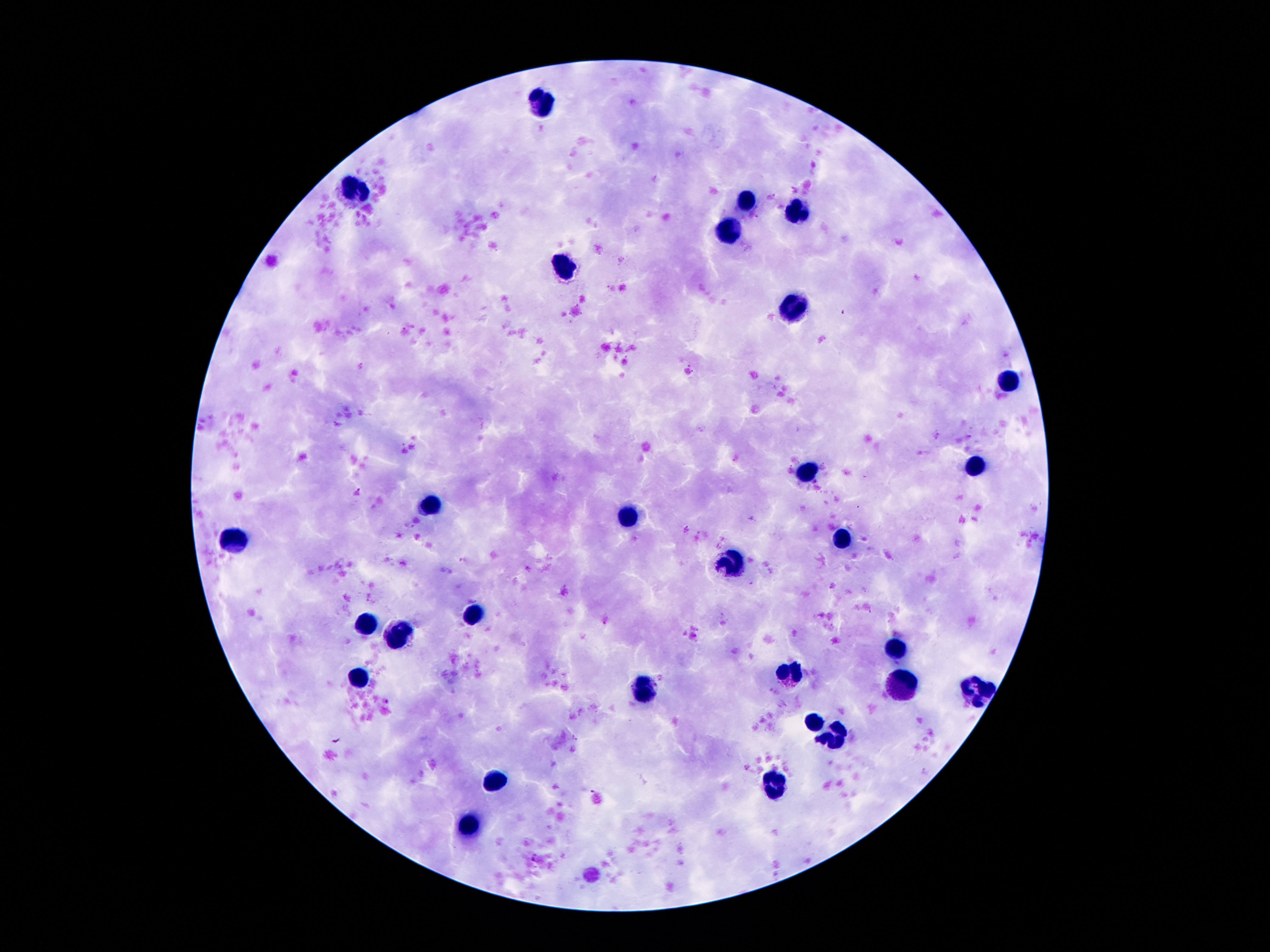 Approximate centers as {x, y} in pixels. Leukocyte locations: {545, 102}, {360, 192}, {745, 202}, {801, 210}, {727, 228}, {566, 265}, {790, 311}, {1004, 378}, {976, 464}, {808, 469}, {430, 504}, {628, 516}, {234, 538}, {841, 538}, {731, 566}, {474, 615}, {365, 625}, {400, 635}, {894, 647}, {791, 674}, {360, 675}, {901, 686}, {645, 690}, {978, 693}, {815, 721}, {838, 739}, {502, 781}, {775, 788}, {470, 823}. Image is 1270×952 pixels. 100x magnification. Patient malaria status: uninfected. Giemsa stain. Thick blood smear. One field from this slide. Photographed through the microscope eyepiece with a smartphone camera.